Assess for Plasmodium parasites.
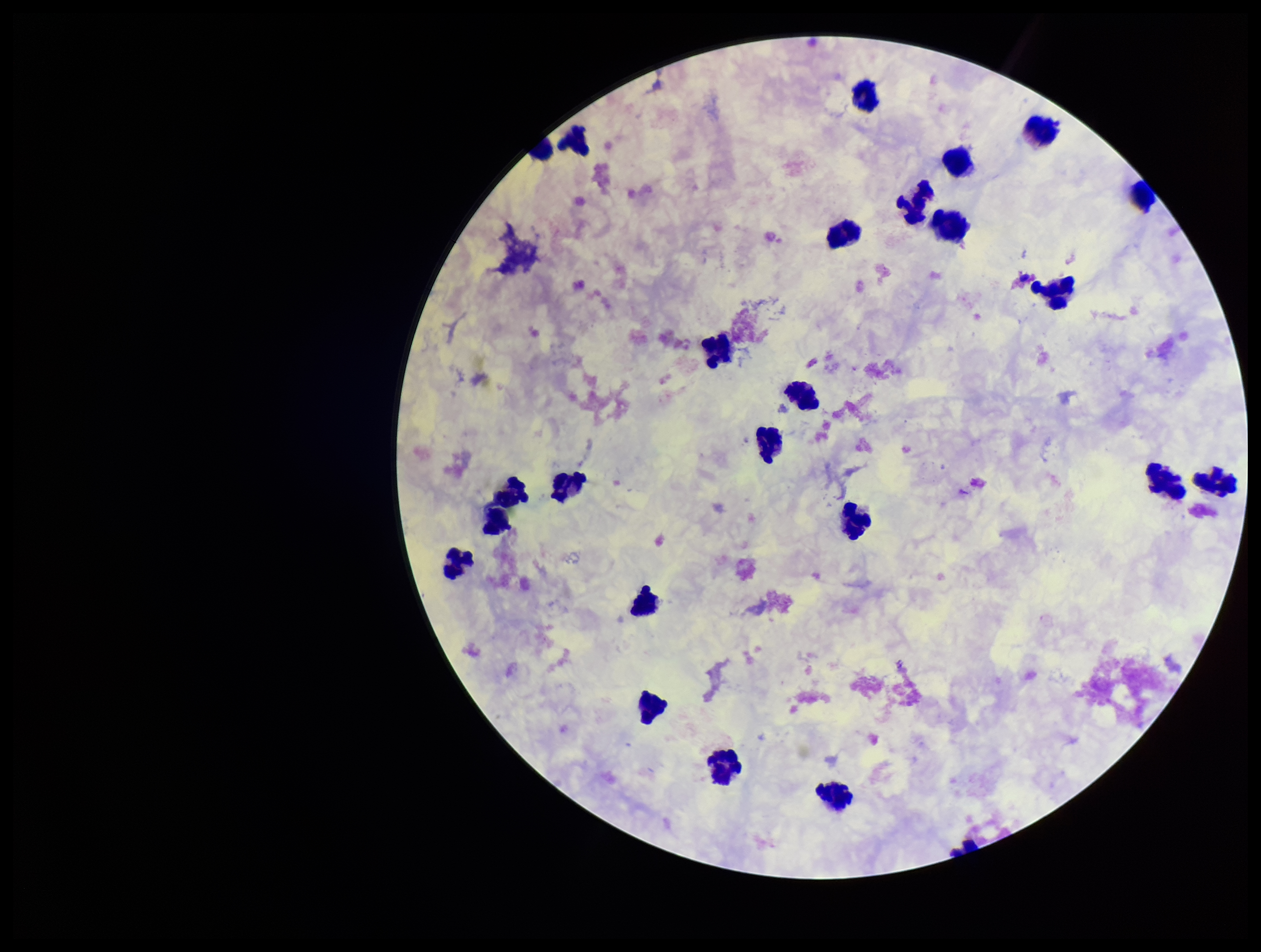
None detected.

Single field of view. Parasite count: 0. Smartphone photograph taken through the eyepiece of a microscope. Leukocyte count: 24. Image is 1261×952 pixels. Patient malaria status: negative. Stained with Giemsa. Preparation: thick smear.